Describe the morphology of the erythrocytes.
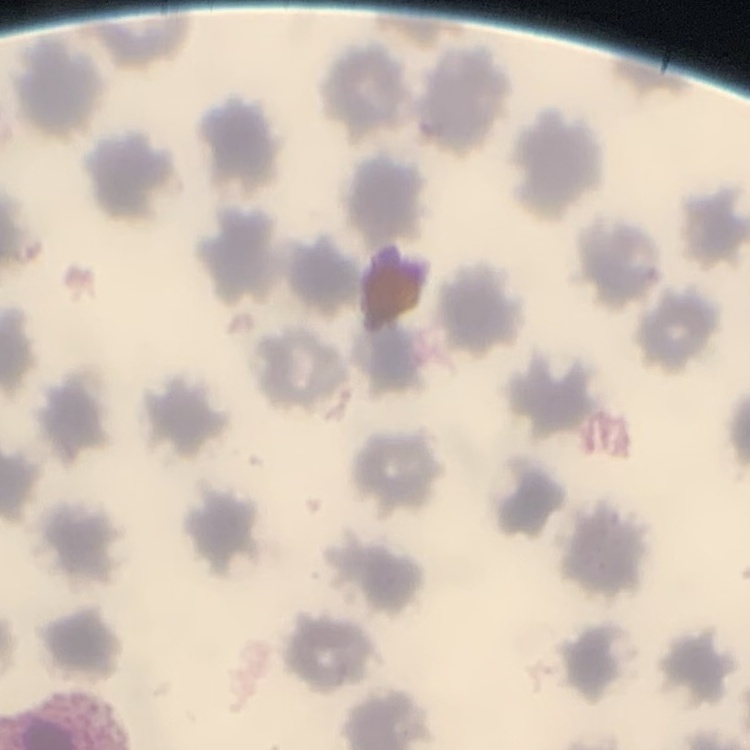
They show no rouleaux formation.

Summary:
  - Image type: square crop of a larger photomicrograph
  - Stain: Field's or Giemsa
  - Preparation: thin blood smear